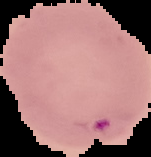
Summary:
  - Image type: segmented cell region with the area outside set to black
  - Malaria status: parasitized
  - Preparation: thin blood smear
  - Image size: 151×157 pixels